Outline each Plasmodium falciparum-infected red blood cell.
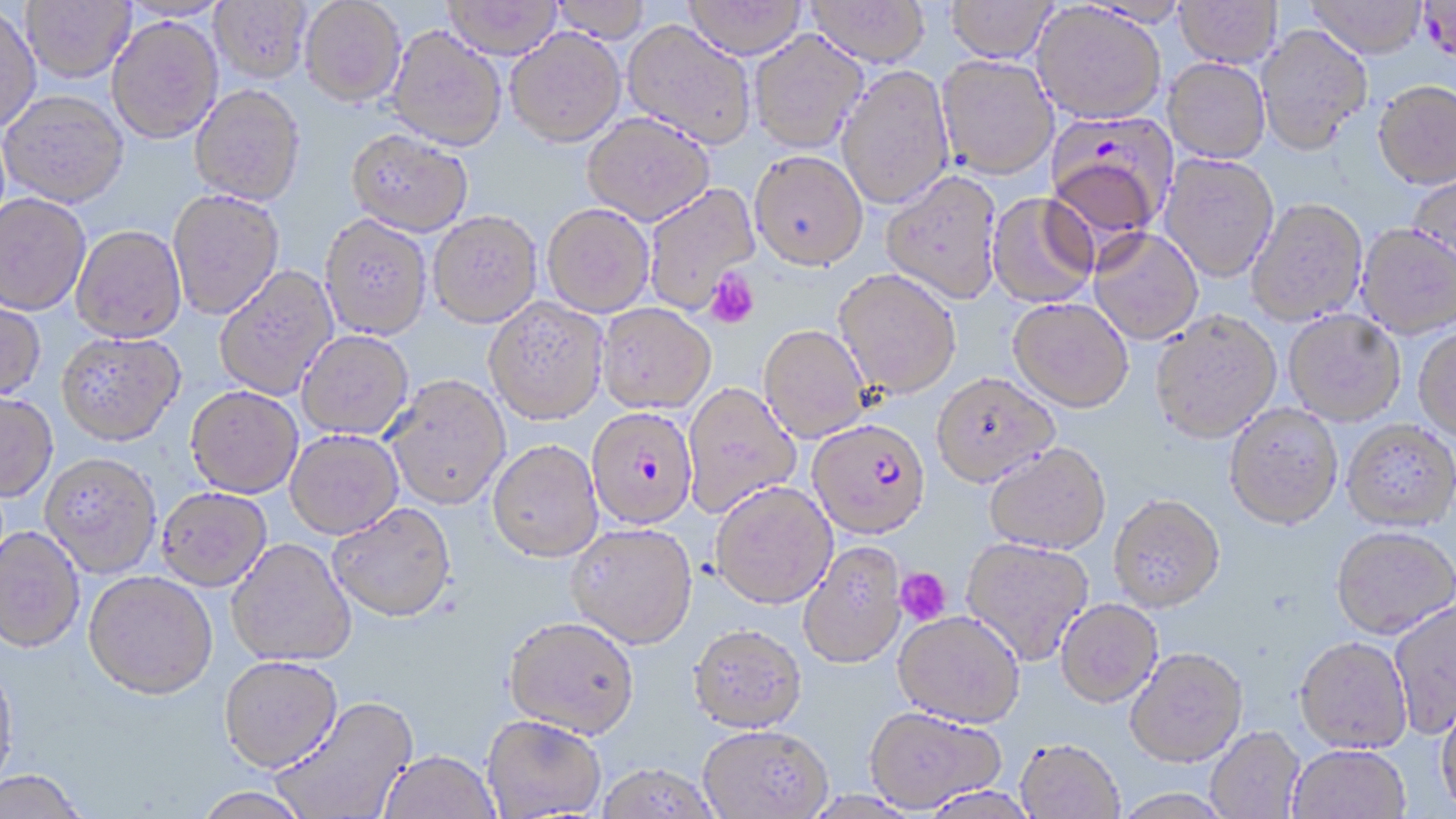

Approximate bounding boxes as (x1,y1)-(x2,y2) corner pairs in pixels.
Plasmodium falciparum-infected red blood cells: (1418,0)-(1456,66), (1044,113)-(1176,241), (585,407)-(697,530), (807,419)-(930,540).

slide-level diagnosis = Plasmodium falciparum
uninfected red blood cell locations = approximate bounding boxes as (x1,y1)-(x2,y2) corner pairs in pixels: (21,0)-(135,82), (210,0)-(312,83), (300,0)-(406,106), (550,0)-(653,42), (443,1)-(563,59), (682,1)-(808,59), (805,1)-(930,66), (945,1)-(1058,63), (1174,1)-(1282,67), (1306,1)-(1427,58), (1031,3)-(1167,125), (0,5)-(41,133), (106,17)-(223,143), (622,19)-(756,150), (1255,23)-(1373,154), (387,24)-(507,152), (506,28)-(626,146), (748,30)-(868,154), (936,54)-(1059,180), (1164,58)-(1270,163), (837,64)-(954,210), (1373,80)-(1456,189), (190,84)-(306,205), (1,90)-(128,207), (581,112)-(715,225), (346,128)-(474,236), (750,150)-(868,270), (1159,152)-(1279,282), (881,171)-(1003,304), (1408,172)-(1456,278), (642,183)-(759,313), (167,189)-(284,319), (0,192)-(91,315), (987,193)-(1098,308), (1245,197)-(1369,325), (542,203)-(654,317), (427,211)-(542,328), (320,215)-(433,340), (1357,222)-(1456,338), (72,225)-(186,343), (1089,228)-(1204,345), (214,265)-(338,400), (833,269)-(962,398), (484,297)-(608,425), (1008,297)-(1134,412), (0,298)-(46,401), (596,303)-(716,414), (1283,309)-(1406,425), (1150,310)-(1282,443), (759,325)-(871,442), (1413,325)-(1456,442), (297,330)-(414,440), (56,331)-(185,445), (931,372)-(1059,487), (384,375)-(511,511), (683,382)-(801,519), (185,386)-(303,498), (0,391)-(58,502), (1224,403)-(1343,529), (1342,419)-(1456,530), (285,430)-(404,540), (487,440)-(603,564), (984,443)-(1111,554), (39,453)-(162,578), (711,482)-(838,609), (156,487)-(273,592), (1109,493)-(1226,611), (328,504)-(457,624), (565,523)-(698,651), (1331,525)-(1455,638), (0,526)-(85,654), (961,537)-(1093,666), (226,539)-(357,668), (797,542)-(907,670), (82,573)-(218,703), (1056,599)-(1162,707), (1388,600)-(1456,739), (893,611)-(1025,728), (503,618)-(640,742), (688,625)-(807,736), (1294,636)-(1412,753), (1126,647)-(1247,767), (219,656)-(344,775), (0,659)-(18,797), (271,696)-(418,819), (1435,697)-(1456,814), (864,708)-(1005,812), (482,716)-(607,818), (698,726)-(832,819), (1206,726)-(1305,818), (1015,740)-(1124,819), (1287,744)-(1410,819), (378,751)-(501,819), (594,764)-(721,819), (0,771)-(88,819), (919,786)-(1041,818), (194,788)-(312,819), (1110,789)-(1234,818)
modality = optical microscopy
platelet locations = approximate bounding boxes as (x1,y1)-(x2,y2) corner pairs in pixels: (704,269)-(760,329), (894,567)-(951,625)
preparation = thin blood film
image size = 1456×819 pixels
stain = May-Grünwald-Giemsa
magnification = 1000x
field of view = single